Classify this cell by malaria status.
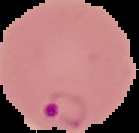
Parasitized.

image type = segmented cell region with the area outside set to black
image size = 139×133 pixels
preparation = thin blood film